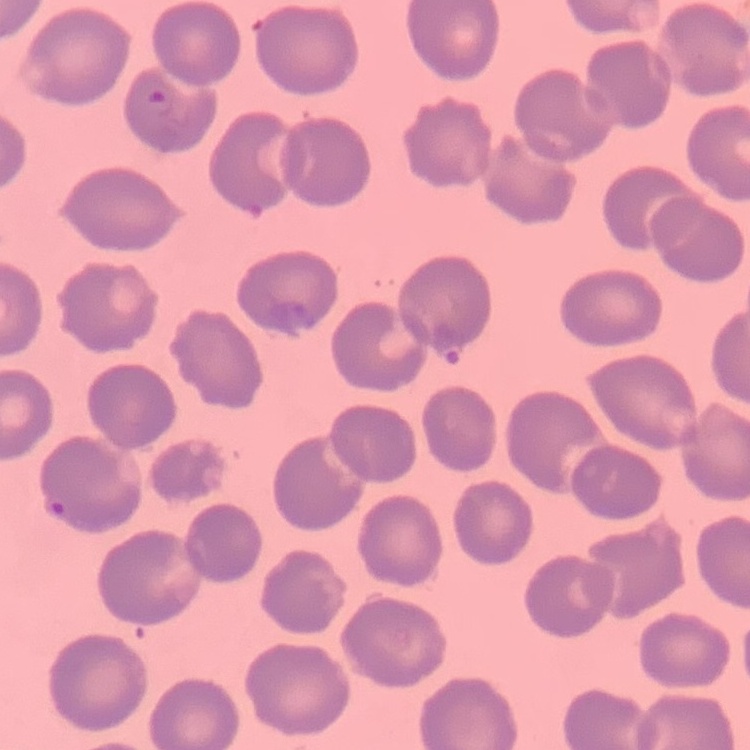

red blood cell morphology = no rouleaux formation
image type = one tile cut from a larger photomicrograph
stain = Field's or Giemsa
preparation = thin peripheral smear